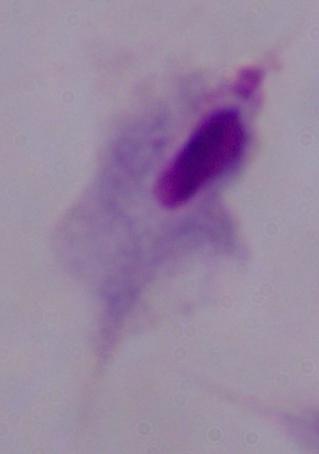
1000x magnification. Photomicrograph. A trichomonad is seen.